Assess this cell for malaria.
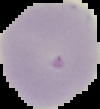
Uninfected.

image size = 100×109 pixels
preparation = thin blood smear
image type = segmented cell region on a black background